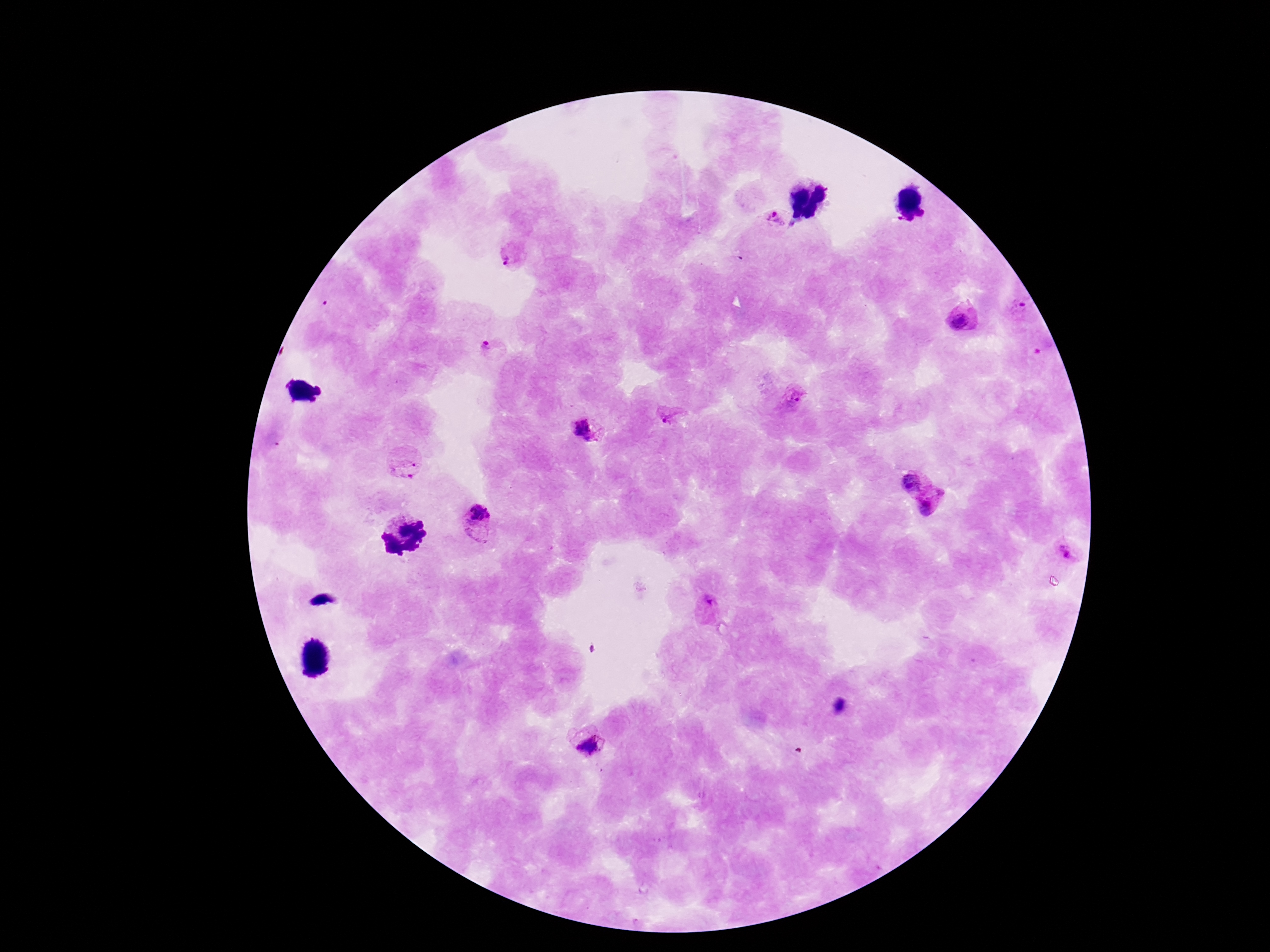

Approximate object centers, in pixels from the top-left corner.
Summary:
  - Plasmodium parasite locations: (x=774, y=219), (x=513, y=253), (x=1019, y=307), (x=962, y=322), (x=485, y=347), (x=793, y=396), (x=671, y=418), (x=584, y=430), (x=404, y=466), (x=909, y=480), (x=934, y=507), (x=479, y=517), (x=1068, y=551), (x=705, y=604), (x=592, y=745)
  - Stain: Giemsa
  - Capture: smartphone camera through the microscope eyepiece
  - Preparation: thick peripheral-blood smear
  - Image size: 1270×952 pixels
  - Patient malaria status: positive
  - Magnification: 100x
  - Field of view: one from this slide